State which parasite is depicted.
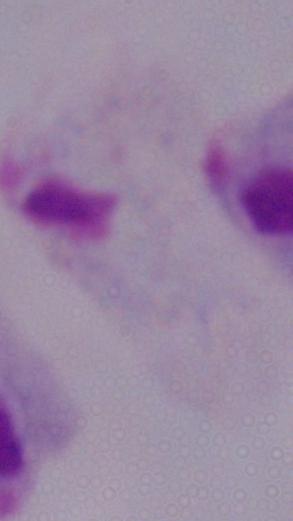
A trichomonad.

modality = photomicrograph
magnification = 1000x